Identify the blood parasite species.
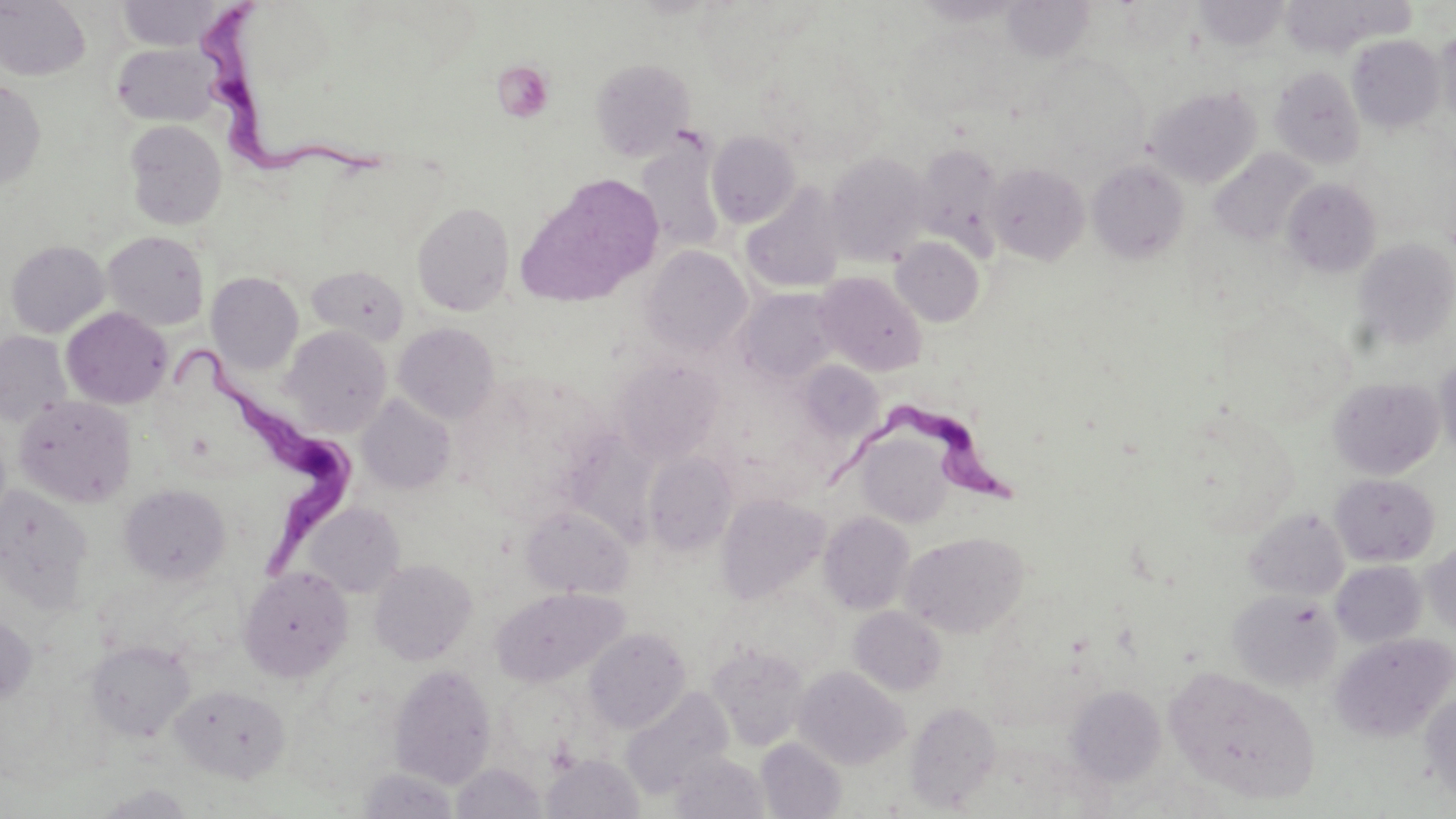
Trypanosoma brucei.

Approximate bounding boxes as (x1,y1)-(x2,y2) corner pairs in pixels. Trypanosoma brucei locations: (205,3)-(379,182), (173,341)-(354,581), (823,401)-(1023,510). Uninfected red blood cell locations (subset): (0,0)-(91,81), (1002,0)-(1094,62), (116,1)-(228,51), (1195,1)-(1289,50), (1435,25)-(1456,130), (896,26)-(1005,117), (1347,35)-(1445,133), (111,43)-(219,126), (759,44)-(886,166), (590,58)-(695,160), (1270,66)-(1366,169), (0,79)-(46,190), (1145,86)-(1260,187), (124,120)-(227,230), (707,131)-(801,227), (636,139)-(726,254), (912,143)-(1005,256), (1209,148)-(1316,247), (824,152)-(931,266), (1088,159)-(1189,264), (986,163)-(1089,264), (516,175)-(663,306), (1282,178)-(1381,276), (741,184)-(845,294), (412,201)-(515,316), (102,231)-(210,331), (891,236)-(985,326), (1352,237)-(1456,352), (5,240)-(110,337), (642,246)-(751,356), (307,265)-(409,346), (814,271)-(927,375), (206,272)-(303,374), (738,288)-(840,383), (61,307)-(172,409), (393,322)-(499,424), (282,326)-(392,436), (0,331)-(73,426), (1435,350)-(1456,464), (613,358)-(723,464), (799,360)-(883,443), (1329,376)-(1444,479), (357,394)-(455,495), (14,396)-(136,508), (858,435)-(952,528), (643,451)-(737,556), (1330,473)-(1440,566), (119,484)-(231,585), (0,486)-(94,610), (717,493)-(829,604), (304,502)-(404,598), (521,505)-(633,598), (1245,508)-(1349,601), (819,511)-(915,615), (901,531)-(1028,638), (1422,541)-(1455,636), (369,558)-(477,665), (1331,560)-(1426,648), (239,566)-(353,682), (492,588)-(627,687), (1228,589)-(1342,690), (849,606)-(946,696), (0,613)-(37,707), (584,628)-(690,732), (1329,632)-(1455,742), (86,640)-(195,741), (707,642)-(811,751), (388,664)-(497,787), (794,666)-(909,769), (1167,667)-(1320,804), (170,683)-(291,783), (1065,684)-(1166,786), (621,687)-(733,797), (1420,689)-(1456,806), (905,701)-(1002,811), (756,738)-(846,819), (669,751)-(769,818), (542,754)-(644,818), (451,762)-(546,818), (358,767)-(460,818), (92,784)-(198,818). Thin blood smear. Light microscopy. May-Grünwald-Giemsa-stained preparation. Image is 1456×819 pixels. Captured at 1000x magnification. Single field of view.